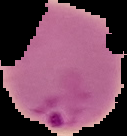 Image is 127×136 pixels. The area outside the segmented cell region is set to black. From a thin blood film. Result: malaria parasites identified.